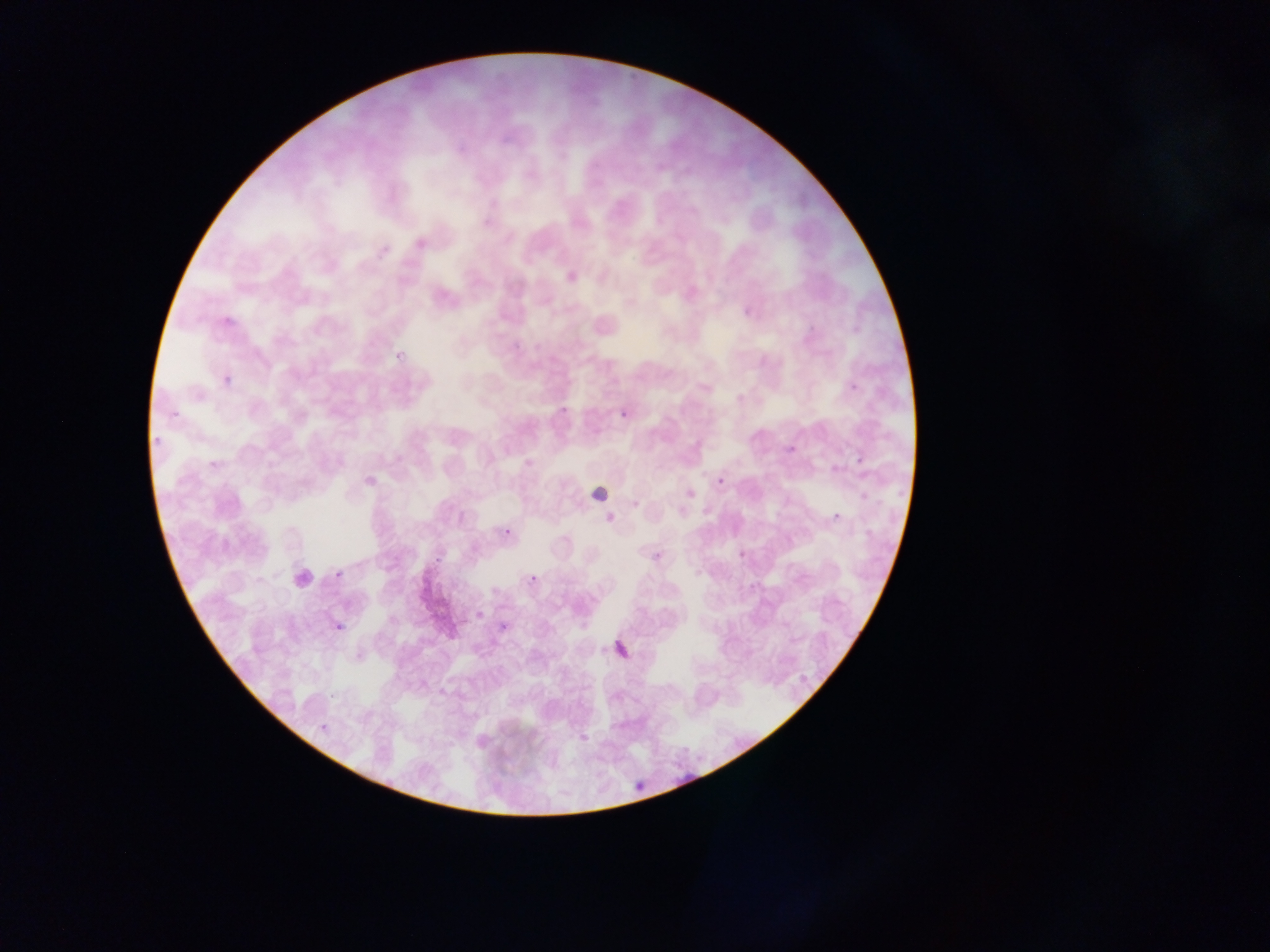
{
  "country": "Ghana",
  "preparation": "thin blood smear",
  "field_of_view": "single",
  "image_size": "1270×952 pixels",
  "malaria_parasite_locations": "approximate bounding boxes as {left, top, right, bottom} in pixels: {388, 347, 414, 363}, {222, 376, 236, 388}, {556, 397, 575, 416}, {615, 399, 638, 421}, {163, 402, 186, 419}, {150, 434, 161, 448}, {783, 442, 808, 459}, {201, 448, 230, 480}, {829, 463, 848, 480}, {715, 476, 725, 486}, {687, 489, 695, 498}, {826, 498, 851, 526}, {703, 505, 712, 514}, {678, 507, 686, 515}, {504, 528, 511, 536}, {332, 564, 344, 588}, {528, 570, 544, 583}, {472, 607, 491, 621}, {331, 614, 351, 634}, {499, 620, 513, 634}, {615, 641, 630, 656}, {626, 769, 654, 793}",
  "capture": "mobile-phone photograph through a microscope"
}